Report the malaria status of this cell.
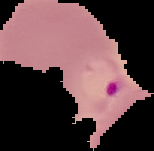
Parasitized.

From a thin blood film. Image is 154×151 pixels. The area outside the segmented cell region is set to black.